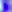
modality = photomicrograph
magnification = 400x
identification = Toxoplasma gondii